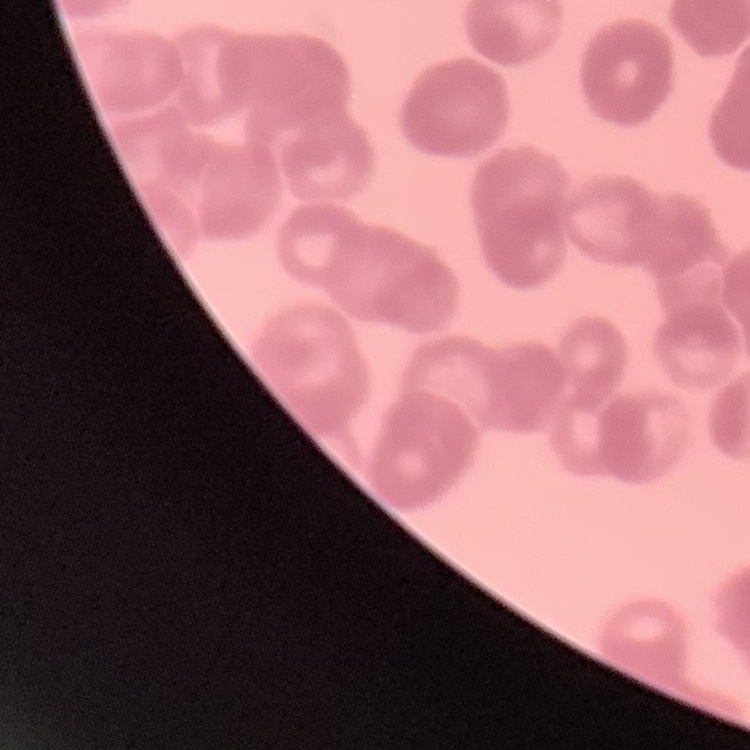
Summary:
  - Red blood cell morphology: rouleaux formation
  - Preparation: thin peripheral smear
  - Image type: one tile cut from a larger photomicrograph
  - Stain: Field's or Giemsa